Give the preparation type.
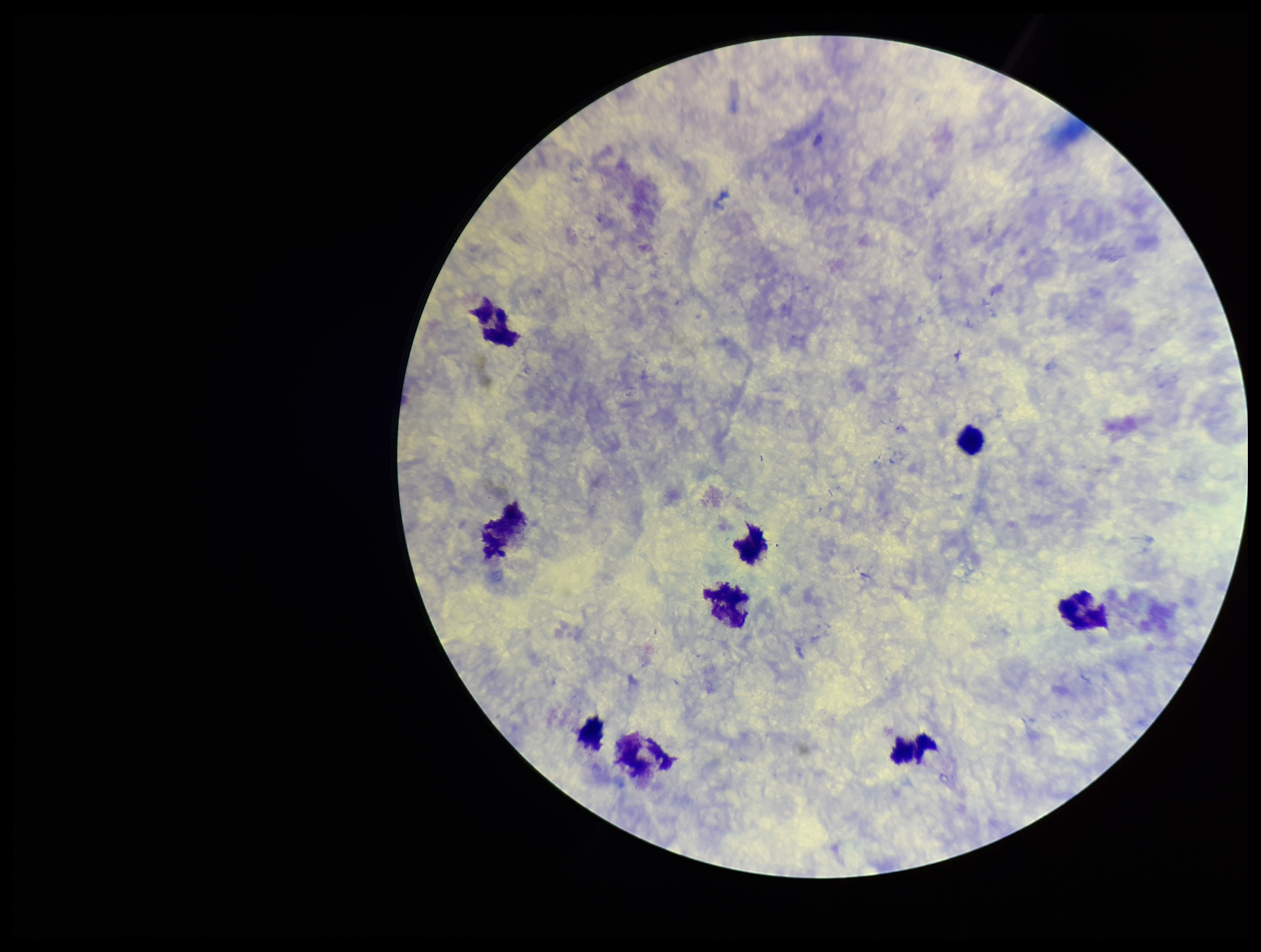
A thick smear.

Stained with Giemsa. Image is 1261×952 pixels. Leukocyte count: 9. Patient malaria status: negative. Parasite count: 0. Single field of view. Plasmodium parasites: none detected. Photographed through the microscope eyepiece with a smartphone camera.